Give the extent of all uninfected red blood cells.
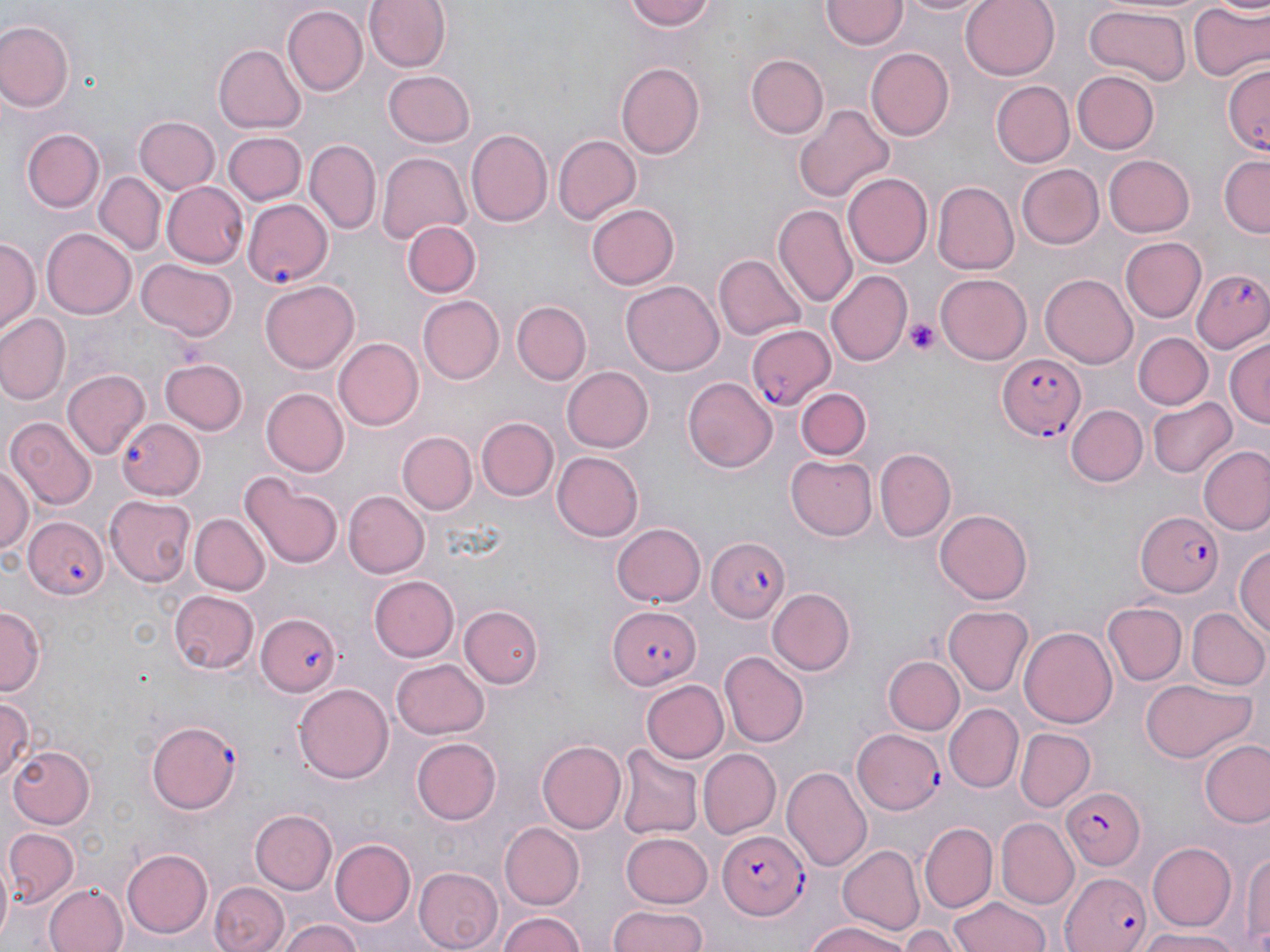

Approximate bounding boxes as named x1/y1/x2/y2 corners in pixels.
Uninfected red blood cells: (x1=363, y1=0, x2=448, y2=74), (x1=621, y1=0, x2=717, y2=32), (x1=895, y1=0, x2=992, y2=18), (x1=961, y1=0, x2=1059, y2=77), (x1=821, y1=1, x2=905, y2=51), (x1=1189, y1=2, x2=1268, y2=83), (x1=281, y1=6, x2=366, y2=96), (x1=1084, y1=7, x2=1190, y2=84), (x1=2, y1=20, x2=76, y2=113), (x1=214, y1=44, x2=306, y2=133), (x1=867, y1=48, x2=955, y2=141), (x1=745, y1=55, x2=828, y2=139), (x1=615, y1=59, x2=704, y2=157), (x1=1224, y1=62, x2=1269, y2=156), (x1=383, y1=70, x2=476, y2=146), (x1=1073, y1=71, x2=1159, y2=153), (x1=992, y1=81, x2=1074, y2=168), (x1=797, y1=102, x2=895, y2=203), (x1=136, y1=117, x2=220, y2=195), (x1=22, y1=129, x2=105, y2=212), (x1=467, y1=129, x2=552, y2=227), (x1=224, y1=132, x2=305, y2=205), (x1=552, y1=134, x2=641, y2=225), (x1=304, y1=140, x2=381, y2=236), (x1=377, y1=152, x2=472, y2=245), (x1=1104, y1=154, x2=1196, y2=236), (x1=1220, y1=157, x2=1269, y2=237), (x1=1015, y1=164, x2=1103, y2=250), (x1=97, y1=171, x2=164, y2=255), (x1=842, y1=173, x2=932, y2=269), (x1=932, y1=181, x2=1018, y2=273), (x1=163, y1=182, x2=249, y2=267), (x1=585, y1=203, x2=680, y2=290), (x1=772, y1=204, x2=858, y2=307), (x1=402, y1=220, x2=480, y2=298), (x1=42, y1=229, x2=135, y2=319), (x1=1121, y1=236, x2=1208, y2=323), (x1=1, y1=238, x2=39, y2=333), (x1=714, y1=254, x2=806, y2=341), (x1=137, y1=258, x2=236, y2=341), (x1=828, y1=271, x2=911, y2=367), (x1=934, y1=272, x2=1031, y2=364), (x1=1041, y1=272, x2=1137, y2=366), (x1=622, y1=280, x2=724, y2=377), (x1=260, y1=281, x2=360, y2=373), (x1=420, y1=295, x2=503, y2=384), (x1=512, y1=301, x2=590, y2=385), (x1=0, y1=314, x2=69, y2=405), (x1=1135, y1=332, x2=1212, y2=410), (x1=334, y1=338, x2=424, y2=429), (x1=1226, y1=339, x2=1270, y2=428), (x1=160, y1=358, x2=249, y2=436), (x1=562, y1=366, x2=653, y2=452), (x1=64, y1=369, x2=150, y2=458), (x1=685, y1=376, x2=779, y2=472), (x1=794, y1=387, x2=872, y2=461), (x1=263, y1=389, x2=349, y2=477), (x1=1147, y1=395, x2=1234, y2=478), (x1=1067, y1=405, x2=1147, y2=487), (x1=476, y1=416, x2=557, y2=499), (x1=7, y1=417, x2=98, y2=510), (x1=396, y1=430, x2=477, y2=514), (x1=1199, y1=444, x2=1270, y2=534), (x1=874, y1=447, x2=955, y2=542), (x1=551, y1=451, x2=643, y2=542), (x1=785, y1=455, x2=875, y2=540), (x1=0, y1=467, x2=34, y2=558), (x1=240, y1=473, x2=344, y2=571), (x1=343, y1=490, x2=429, y2=577), (x1=106, y1=493, x2=195, y2=586), (x1=935, y1=510, x2=1033, y2=603), (x1=189, y1=513, x2=269, y2=595), (x1=611, y1=522, x2=705, y2=608), (x1=1235, y1=542, x2=1270, y2=642), (x1=369, y1=575, x2=458, y2=661), (x1=767, y1=588, x2=857, y2=674), (x1=167, y1=589, x2=261, y2=674), (x1=0, y1=603, x2=45, y2=693), (x1=1104, y1=603, x2=1186, y2=685), (x1=459, y1=604, x2=542, y2=688), (x1=944, y1=604, x2=1032, y2=695), (x1=1187, y1=608, x2=1269, y2=691), (x1=1021, y1=624, x2=1118, y2=731), (x1=719, y1=652, x2=809, y2=747), (x1=883, y1=655, x2=965, y2=736), (x1=392, y1=658, x2=489, y2=738), (x1=1141, y1=677, x2=1251, y2=762), (x1=644, y1=679, x2=728, y2=763), (x1=292, y1=683, x2=394, y2=784), (x1=0, y1=696, x2=37, y2=784), (x1=946, y1=702, x2=1023, y2=792), (x1=1015, y1=728, x2=1095, y2=811), (x1=412, y1=738, x2=502, y2=824), (x1=536, y1=740, x2=625, y2=835), (x1=1200, y1=741, x2=1270, y2=827), (x1=615, y1=742, x2=701, y2=840), (x1=7, y1=745, x2=97, y2=830), (x1=697, y1=748, x2=779, y2=837), (x1=784, y1=765, x2=873, y2=869), (x1=250, y1=808, x2=338, y2=893), (x1=997, y1=818, x2=1079, y2=911), (x1=920, y1=822, x2=996, y2=913), (x1=502, y1=823, x2=585, y2=909), (x1=5, y1=828, x2=78, y2=904), (x1=620, y1=831, x2=712, y2=907), (x1=331, y1=837, x2=416, y2=925), (x1=1148, y1=842, x2=1239, y2=930), (x1=838, y1=843, x2=922, y2=934), (x1=1242, y1=845, x2=1270, y2=952), (x1=122, y1=849, x2=213, y2=937), (x1=9, y1=850, x2=99, y2=943), (x1=0, y1=856, x2=16, y2=945), (x1=410, y1=866, x2=502, y2=952), (x1=211, y1=879, x2=288, y2=951), (x1=45, y1=884, x2=127, y2=952), (x1=950, y1=897, x2=1052, y2=952), (x1=605, y1=907, x2=714, y2=951), (x1=495, y1=910, x2=589, y2=952), (x1=280, y1=919, x2=364, y2=952), (x1=800, y1=920, x2=916, y2=952), (x1=901, y1=925, x2=957, y2=952), (x1=1138, y1=928, x2=1244, y2=951).

Platelet locations: (x1=905, y1=320, x2=942, y2=356). Plasmodium falciparum-infected red blood cell locations: (x1=243, y1=197, x2=334, y2=287), (x1=1192, y1=268, x2=1270, y2=354), (x1=745, y1=322, x2=835, y2=412), (x1=996, y1=353, x2=1084, y2=439), (x1=117, y1=417, x2=204, y2=498), (x1=1135, y1=510, x2=1222, y2=597), (x1=23, y1=516, x2=108, y2=601), (x1=706, y1=536, x2=789, y2=623), (x1=605, y1=606, x2=701, y2=691), (x1=255, y1=611, x2=341, y2=697), (x1=147, y1=721, x2=239, y2=813), (x1=853, y1=729, x2=943, y2=814), (x1=1063, y1=786, x2=1146, y2=872), (x1=719, y1=829, x2=807, y2=919), (x1=1063, y1=871, x2=1154, y2=952). Slide-level diagnosis: Plasmodium falciparum. Thin blood smear. Optical microscopy. Image is 1270×952 pixels. Single field of view. 1000x magnification. May-Grünwald-Giemsa stain.